Assess this cell for malaria.
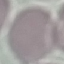

Uninfected.

Cell patch, automatically extracted from a larger field of view and resized to 64 × 64 pixels. Giemsa stain. Photographed with a smartphone camera at the microscope eyepiece. Thin smear of blood.